Report the malaria status of this cell.
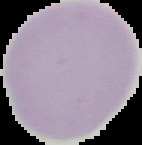

It is uninfected.

Summary:
  - Preparation: thin blood film
  - Image type: cell region segmented out of the field of view; surrounding area masked to black
  - Image size: 142×145 pixels